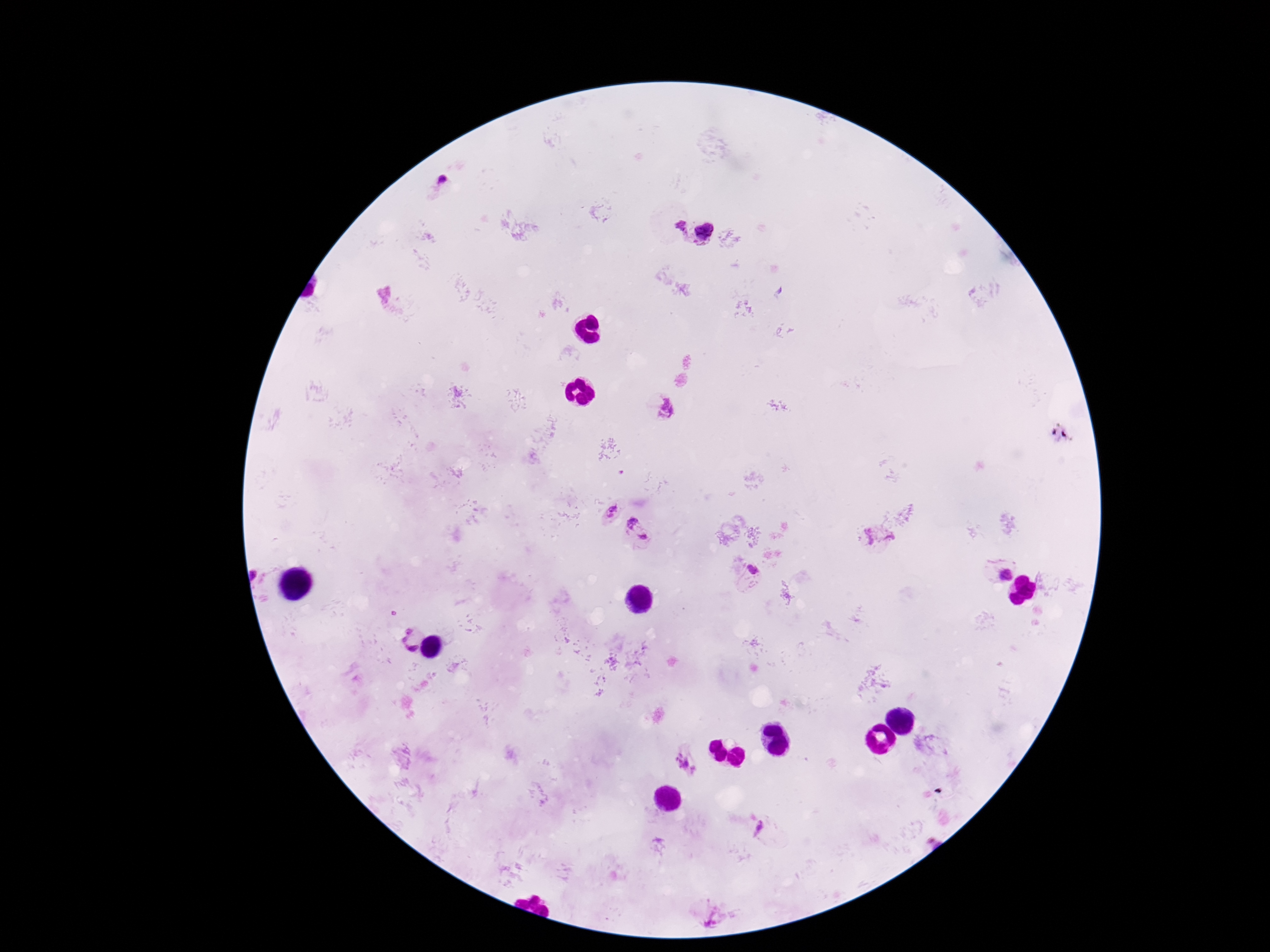

Approximate centers as [x, y] in pixels. Plasmodium parasite locations: [444, 178], [680, 229], [707, 232], [668, 408], [609, 511], [632, 523], [868, 537], [889, 537], [644, 538], [753, 570], [1004, 573], [255, 576], [409, 642], [685, 764], [760, 831]. Giemsa stain. Thick blood smear. 100x magnification. Photographed through the microscope eyepiece with a smartphone camera. Image is 1270×952 pixels. Patient malaria status: positive. Single field of view.